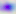
{
  "magnification": "400x",
  "modality": "micrograph",
  "identification": "Toxoplasma gondii"
}